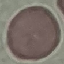
result = no malaria parasites seen
stain = Giemsa
capture = smartphone through the microscope eyepiece
image type = automatically extracted cell patch, resized to 64 × 64 pixels
preparation = thin blood smear